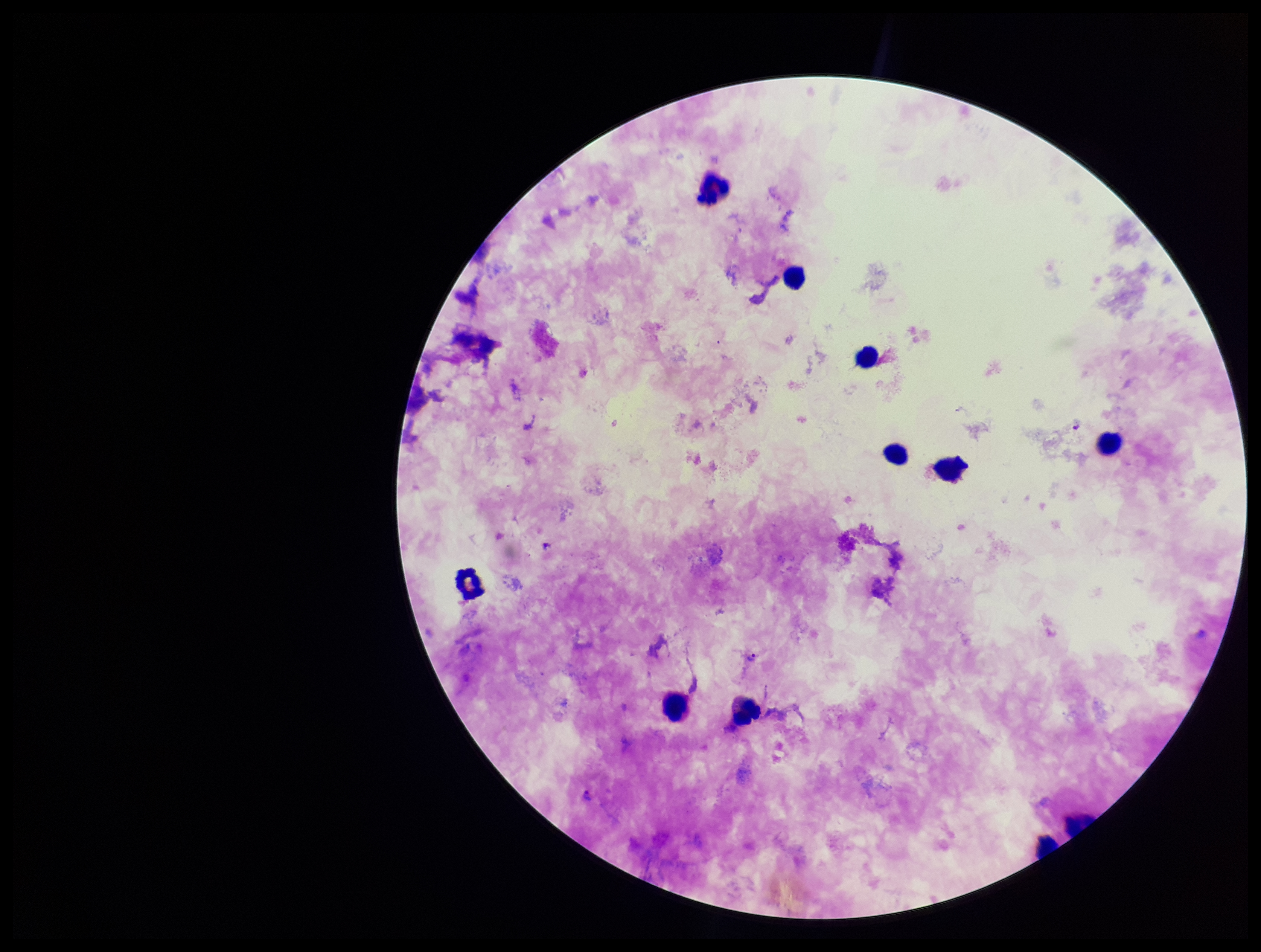

Summary:
  - Field of view: one from this slide
  - Preparation: thick blood smear
  - Parasite count: 2
  - Patient malaria status: infected
  - Image size: 1261×952 pixels
  - Species reported for this patient: Plasmodium falciparum
  - Plasmodium parasites: detected
  - Stain: Giemsa
  - Leukocyte count: 11
  - Capture: smartphone photograph through the microscope eyepiece